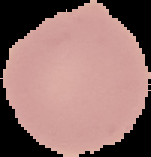
Summary:
  - Image type: segmented cell region on a black background
  - Malaria status: uninfected
  - Image size: 151×157 pixels
  - Preparation: thin blood film